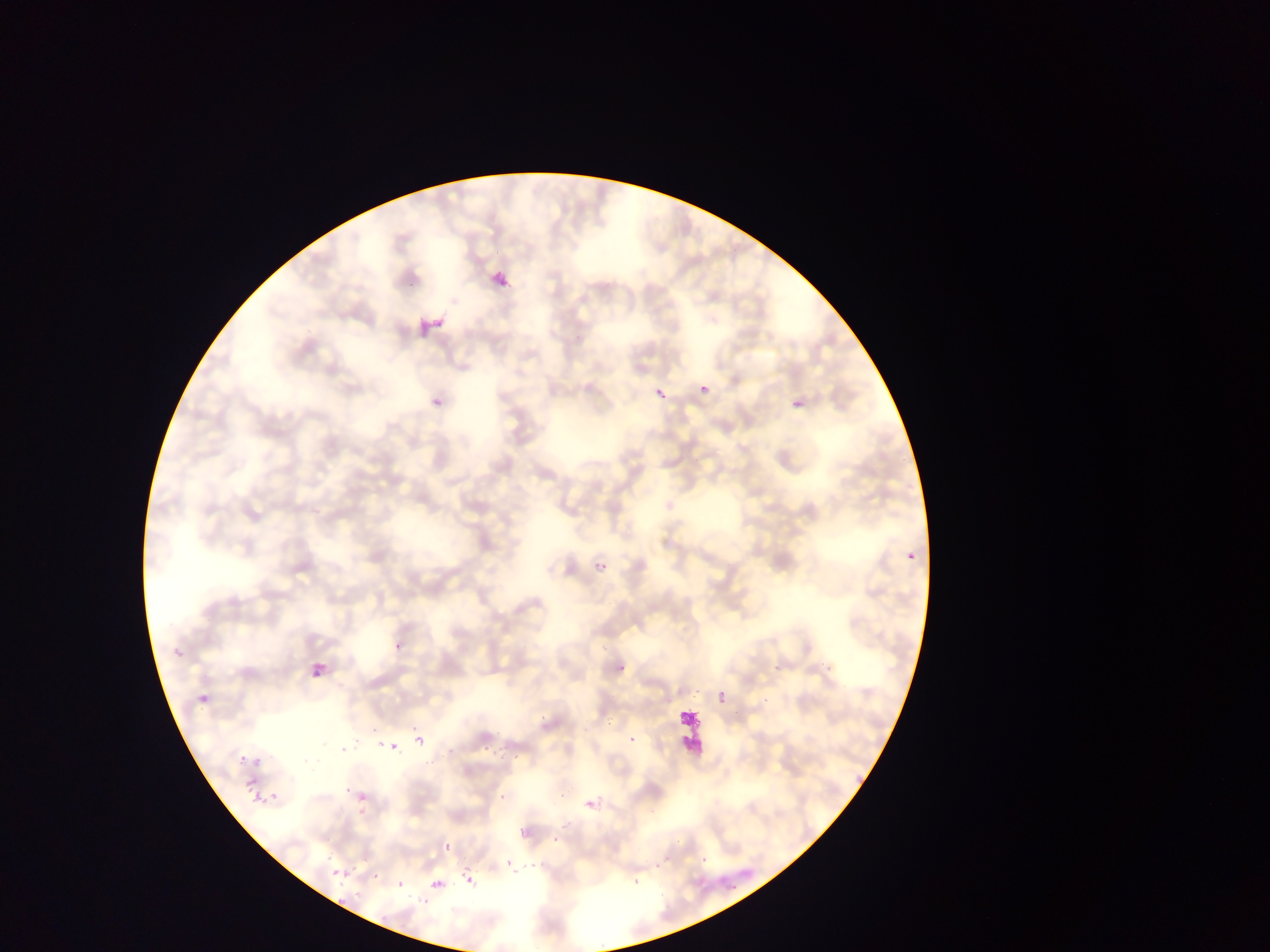
{
  "plasmodium_parasite_locations": "approximate bounding boxes as (left, top, right, bottom) in pixels: (450, 297, 459, 306), (417, 314, 442, 335), (428, 315, 445, 333), (435, 317, 444, 329), (416, 320, 434, 335), (652, 381, 669, 397), (699, 384, 710, 394), (791, 397, 804, 410), (431, 400, 443, 412), (905, 550, 916, 562), (586, 554, 614, 571), (395, 641, 402, 652), (175, 649, 184, 658), (767, 651, 788, 676), (818, 652, 837, 668), (613, 660, 630, 681), (310, 663, 328, 678), (715, 674, 727, 705), (689, 685, 707, 703), (761, 689, 774, 706), (193, 697, 210, 711), (604, 708, 621, 733), (538, 713, 547, 722), (623, 730, 637, 749), (382, 731, 404, 762), (366, 733, 382, 746), (412, 734, 424, 748), (339, 737, 354, 754), (447, 743, 458, 760), (486, 748, 503, 758), (423, 751, 438, 769), (235, 752, 247, 769), (509, 753, 521, 761), (252, 755, 265, 766), (239, 779, 258, 789), (337, 785, 349, 796), (354, 785, 371, 802), (556, 785, 568, 803), (244, 793, 258, 807), (268, 793, 278, 806), (580, 793, 597, 811), (498, 794, 508, 803), (356, 806, 371, 820), (550, 834, 561, 845), (442, 838, 453, 859), (695, 849, 712, 866), (320, 851, 331, 863), (651, 856, 668, 871), (343, 858, 352, 881), (501, 858, 523, 877), (531, 864, 543, 876), (462, 865, 479, 884), (371, 870, 383, 882), (327, 873, 341, 891), (398, 873, 406, 885), (431, 879, 443, 889), (628, 879, 645, 889), (725, 880, 739, 893), (420, 892, 435, 920), (405, 894, 416, 907), (331, 899, 346, 908)",
  "field_of_view": "single",
  "artifact_stain_precipitate_or_debris_locations": "approximate bounding boxes as (left, top, right, bottom) in pixels: (670, 711, 703, 762)",
  "image_size": "1270×952 pixels",
  "country": "Ghana",
  "preparation": "thin blood film",
  "capture": "mobile-phone photograph through a microscope"
}